Classify this cell by malaria status.
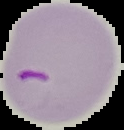

Parasitized.

image type = segmented cell region on a black background
preparation = thin blood smear
image size = 124×130 pixels